Assess the morphology of the red blood cells.
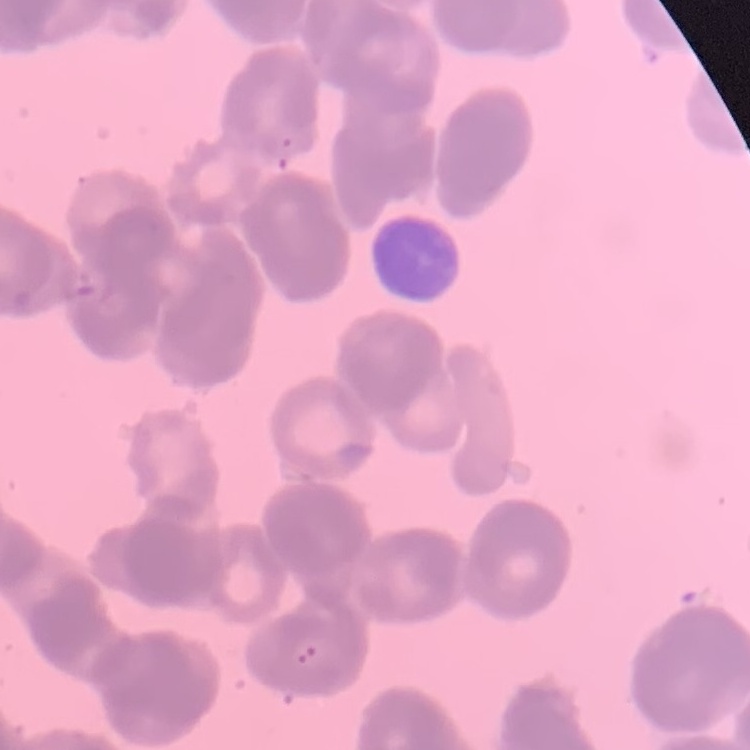

They show rouleaux formation.

Thin blood film. Field's or Giemsa stain. One tile cut from a larger photomicrograph.